State which parasite is depicted.
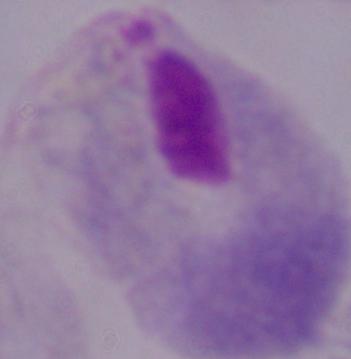
A trichomonad.

modality = micrograph
magnification = 1000x